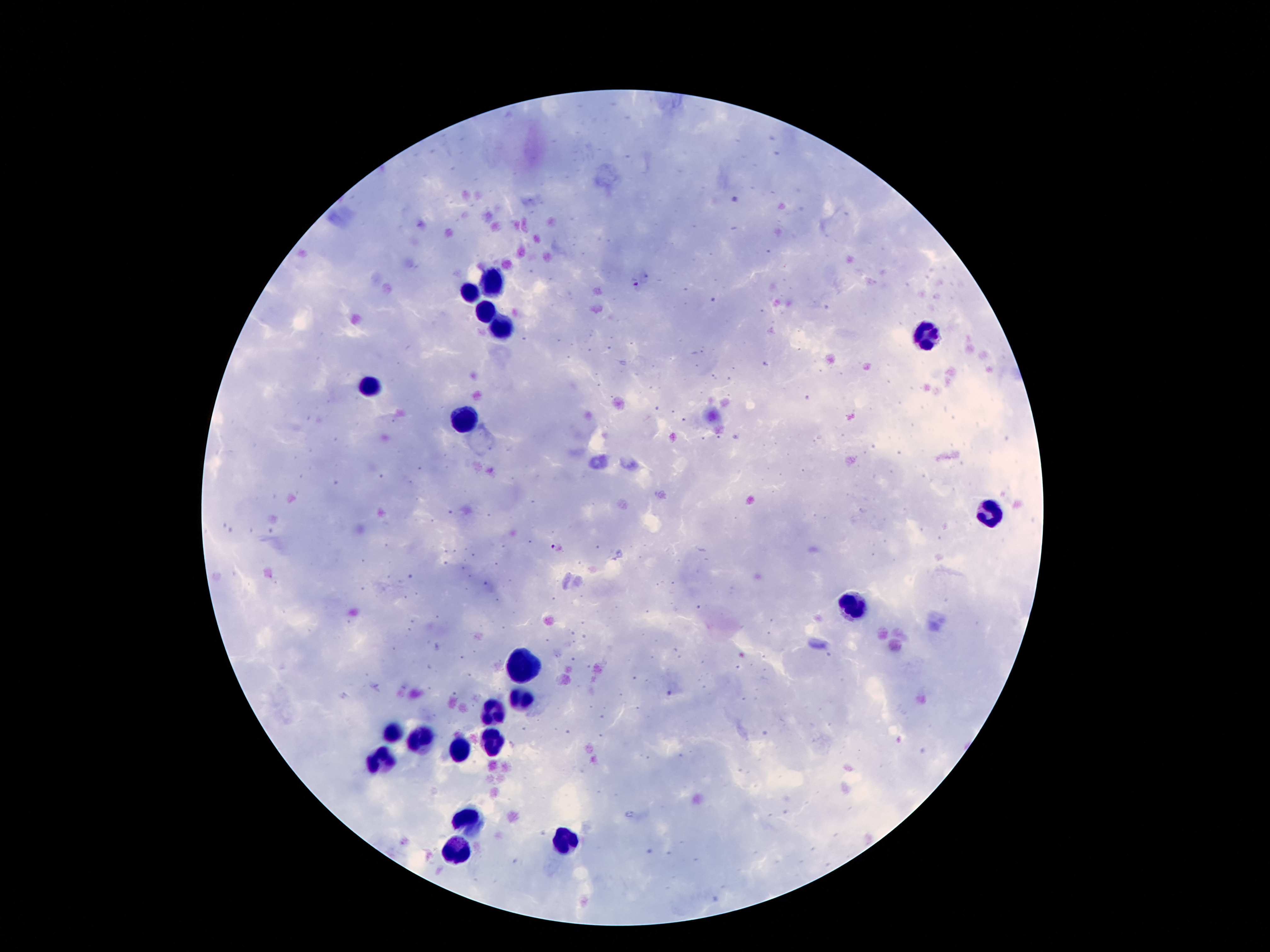
coordinate format = approximate centers as [x, y] in pixels
leukocyte locations = [491, 282], [470, 294], [482, 311], [500, 325], [923, 332], [371, 385], [467, 419], [990, 512], [855, 607], [522, 669], [518, 699], [494, 711], [393, 732], [419, 739], [493, 739], [460, 750], [381, 759], [472, 821], [568, 842], [458, 847]
malaria parasite locations = [635, 281], [552, 547]
magnification = 100x
preparation = thick blood smear
stain = Giemsa
capture = smartphone through the microscope eyepiece
image size = 1270×952 pixels
field of view = one from this slide
patient malaria status = positive for Plasmodium falciparum